Identify the parasite.
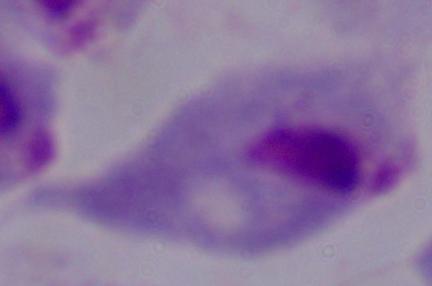

This is a trichomonad.

magnification = 1000x
modality = micrograph